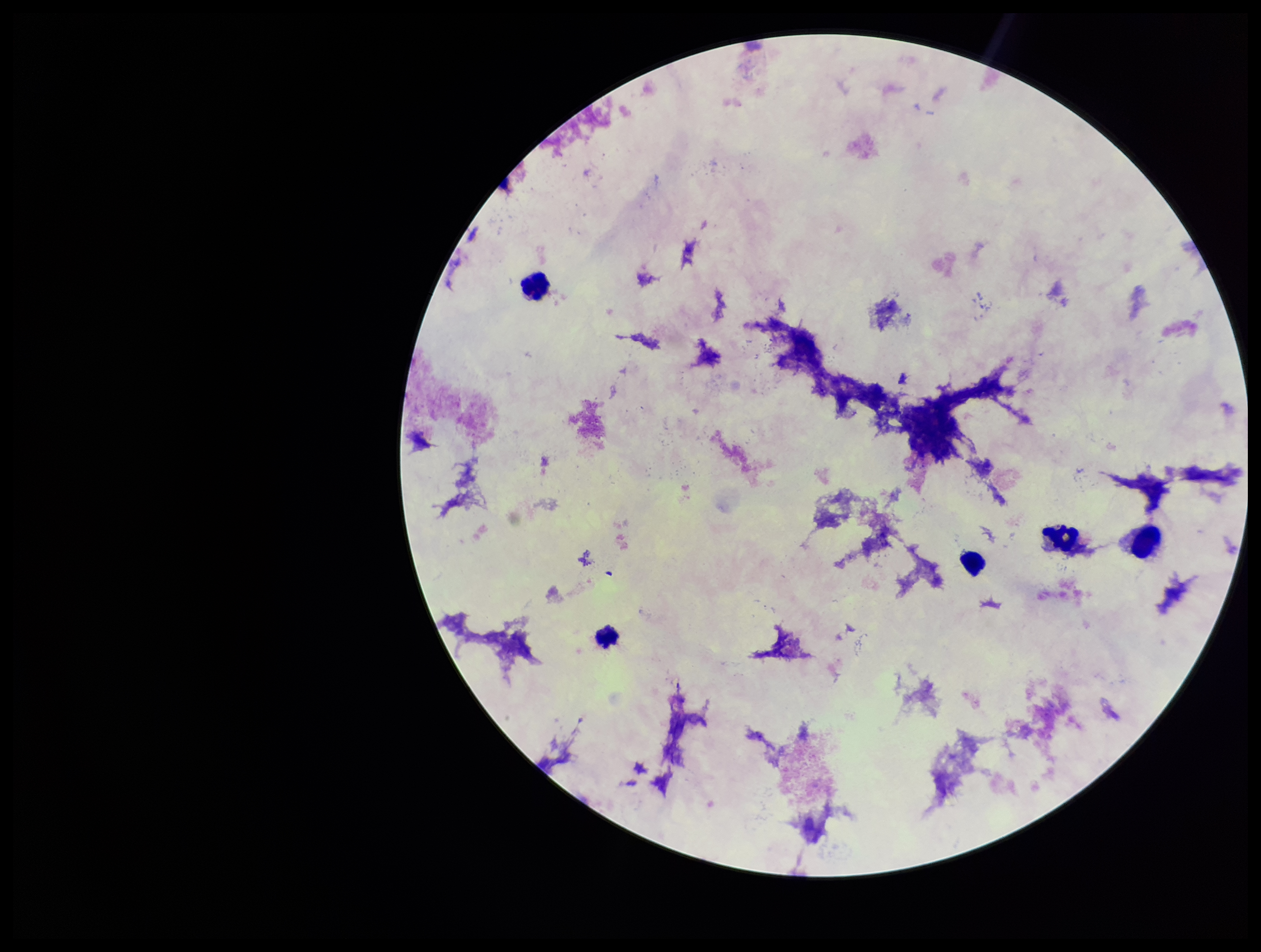

leukocyte count = 5
image size = 1261×952 pixels
patient malaria status = negative
capture = smartphone photograph through the microscope eyepiece
parasite count = 0
preparation = thick smear
stain = Giemsa
Plasmodium parasites = none identified
field of view = one from this slide